Name the blood parasite species.
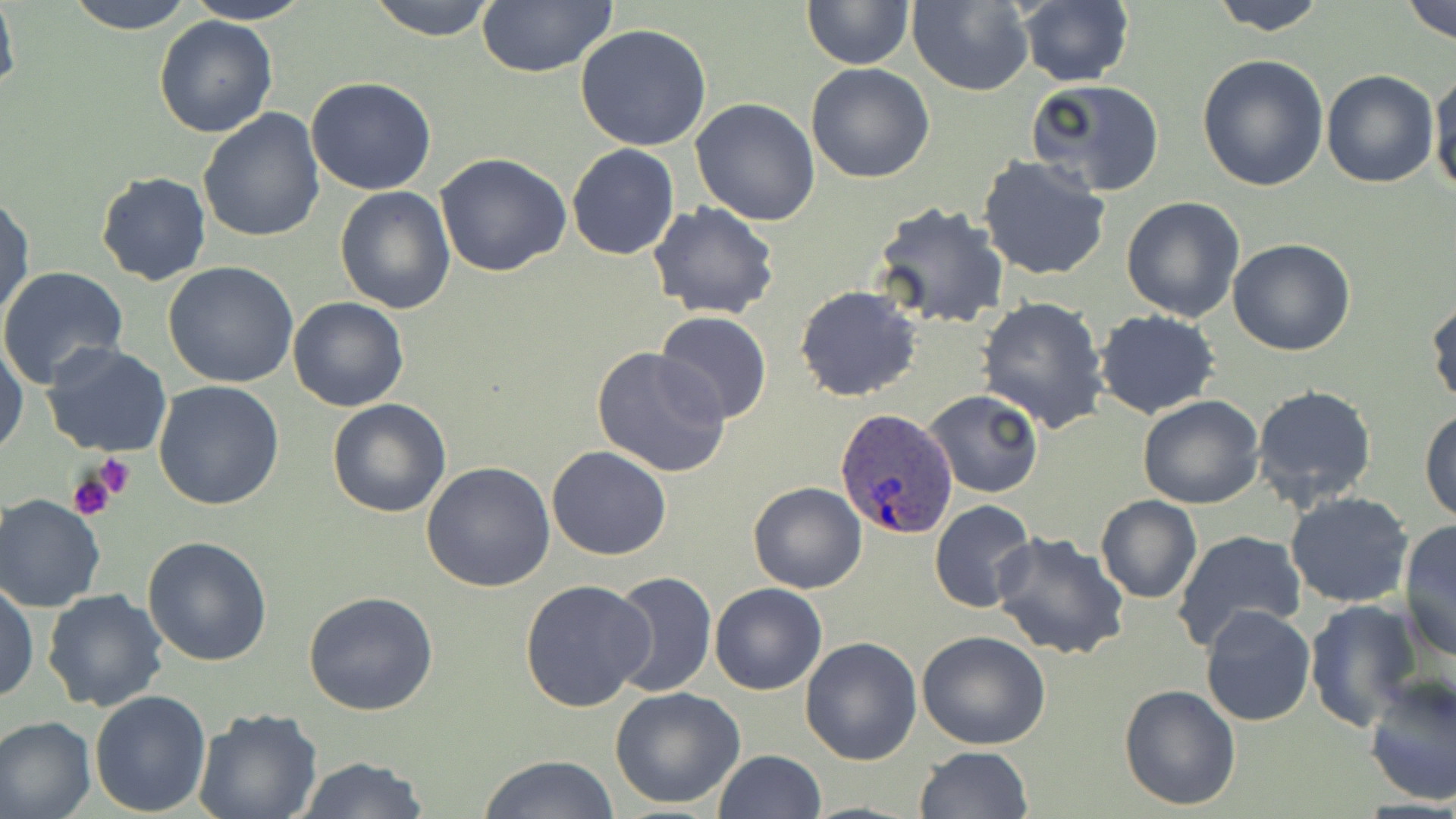
Plasmodium ovale.

field of view = single
Plasmodium ovale-infected red blood cell locations = approximate bounding boxes as (x1,y1)-(x2,y2) corner pairs in pixels: (832,408)-(959,540)
platelet locations = approximate bounding boxes as (x1,y1)-(x2,y2) corner pairs in pixels: (94,456)-(137,500), (67,468)-(122,522)
preparation = thin blood film
magnification = 1000x
uninfected red blood cell locations = approximate bounding boxes as (x1,y1)-(x2,y2) corner pairs in pixels: (0,0)-(21,102), (64,0)-(199,34), (181,0)-(316,24), (366,0)-(500,40), (801,0)-(913,69), (1207,0)-(1330,34), (1402,0)-(1456,43), (475,1)-(620,77), (906,1)-(1034,94), (1015,1)-(1134,87), (152,14)-(278,138), (574,24)-(713,151), (1196,54)-(1329,193), (805,62)-(935,183), (1429,69)-(1456,197), (1320,70)-(1439,188), (306,77)-(436,195), (1027,78)-(1166,197), (690,98)-(823,226), (198,108)-(325,246), (567,144)-(680,260), (434,153)-(572,277), (977,155)-(1113,280), (95,171)-(213,287), (335,186)-(456,314), (0,191)-(35,325), (1120,195)-(1247,322), (647,200)-(779,320), (871,201)-(1009,332), (1228,238)-(1355,357), (163,262)-(300,388), (0,266)-(130,387), (795,285)-(922,401), (1426,294)-(1456,408), (287,295)-(409,413), (976,296)-(1109,434), (1093,309)-(1221,420), (654,311)-(774,426), (0,337)-(28,459), (40,341)-(175,459), (589,346)-(732,480), (153,381)-(286,510), (1251,384)-(1379,510), (923,389)-(1044,497), (1137,394)-(1266,510), (327,398)-(451,518), (1419,407)-(1456,525), (547,446)-(672,561), (421,461)-(555,592), (748,482)-(867,594), (1284,491)-(1415,610), (1,495)-(105,612), (1095,495)-(1203,604), (930,500)-(1039,615), (1398,519)-(1456,662), (988,529)-(1133,661), (1171,529)-(1306,651), (142,535)-(276,667), (608,571)-(717,698), (518,578)-(655,712), (1,581)-(38,704), (709,583)-(828,696), (41,589)-(169,713), (304,592)-(439,716), (1304,599)-(1422,729), (1200,604)-(1316,727), (755,611)-(893,750), (917,630)-(1051,750), (799,636)-(922,765), (1361,674)-(1456,807), (1118,683)-(1241,811), (610,686)-(748,809), (89,690)-(213,816), (193,708)-(324,819), (0,715)-(97,819), (916,746)-(1034,818), (713,749)-(826,819), (478,754)-(619,819), (294,756)-(430,819)
image size = 1456×819 pixels
stain = May-Grünwald-Giemsa
modality = light microscopy